Identify the cell.
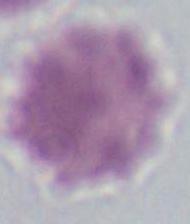

An erythrocyte.

Summary:
  - Magnification: 1000x
  - Modality: photomicrograph